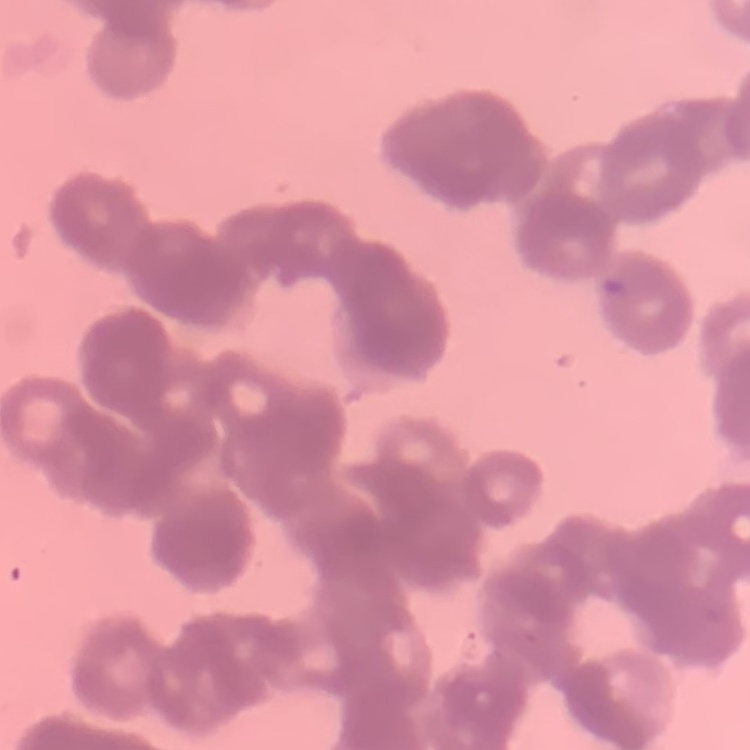
Summary:
  - Erythrocyte morphology: rouleaux formation
  - Preparation: thin blood smear
  - Image type: square crop of a larger photomicrograph
  - Stain: Field's or Giemsa